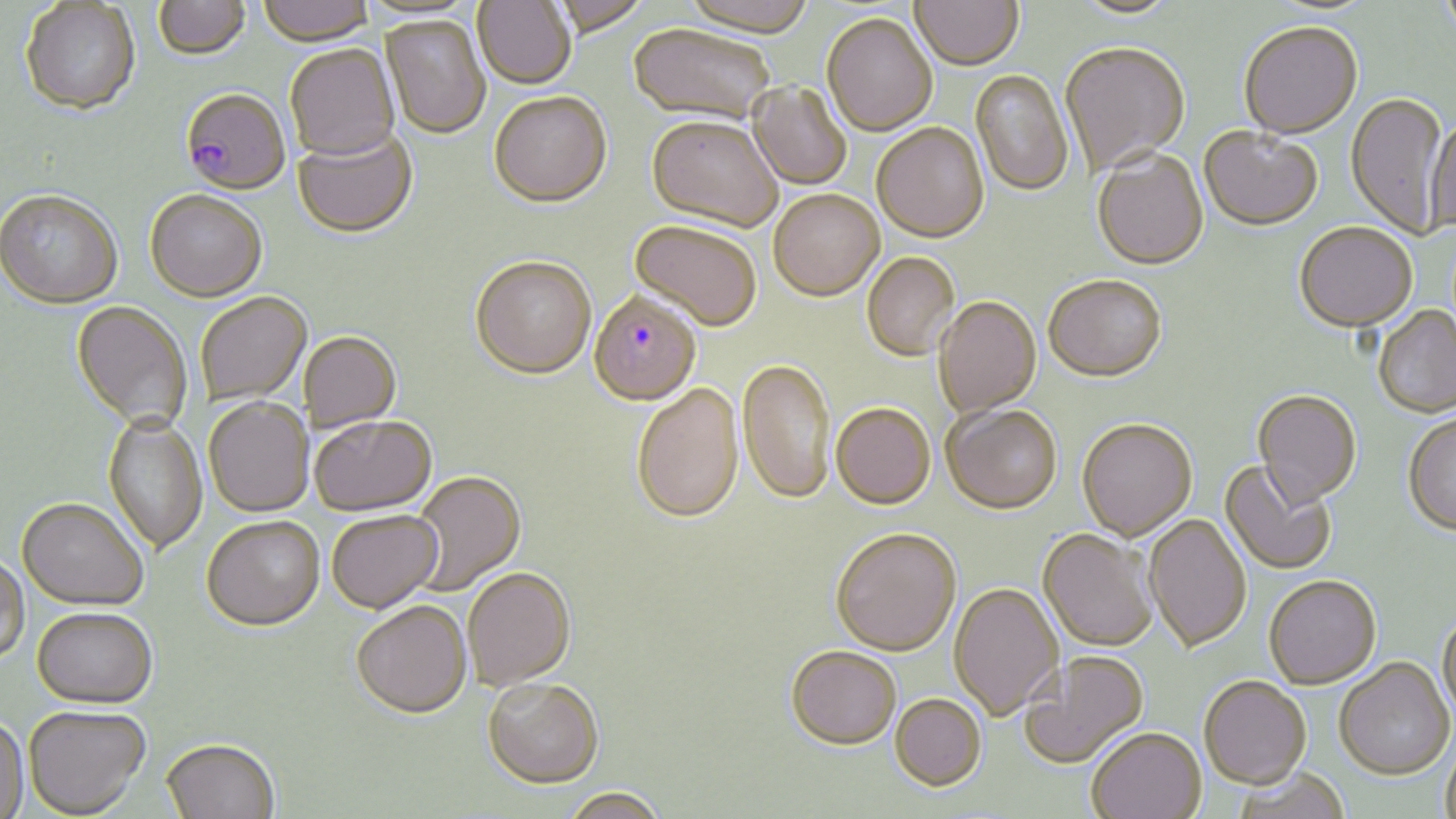
Approximate bounding boxes as [x1, y1, x2, y2] in pixels. Plasmodium falciparum-infected red blood cell locations: [179, 91, 290, 198], [588, 295, 702, 409]. Uninfected red blood cell locations: [256, 0, 376, 48], [472, 0, 576, 91], [680, 0, 819, 40], [910, 0, 1024, 73], [1438, 0, 1456, 44], [153, 1, 251, 62], [1071, 1, 1183, 20], [20, 2, 141, 118], [821, 16, 937, 139], [380, 17, 491, 140], [1239, 24, 1363, 142], [628, 26, 774, 128], [1060, 45, 1190, 178], [285, 47, 401, 164], [970, 70, 1073, 199], [748, 82, 851, 191], [1346, 93, 1449, 240], [490, 95, 612, 211], [1426, 118, 1456, 236], [646, 119, 782, 235], [871, 125, 989, 246], [1199, 129, 1323, 233], [292, 131, 419, 241], [1092, 151, 1209, 272], [0, 193, 123, 312], [145, 193, 267, 305], [769, 193, 884, 304], [628, 222, 761, 335], [1294, 224, 1417, 334], [862, 254, 960, 363], [470, 259, 596, 383], [1043, 278, 1167, 385], [197, 294, 312, 407], [934, 298, 1042, 419], [70, 303, 192, 434], [1374, 306, 1456, 418], [300, 333, 402, 434], [738, 360, 835, 508], [632, 386, 744, 527], [1252, 391, 1362, 510], [203, 400, 314, 519], [831, 406, 935, 512], [942, 407, 1062, 517], [1402, 414, 1456, 537], [102, 415, 208, 557], [311, 418, 438, 520], [1076, 421, 1197, 543], [1220, 459, 1336, 575], [409, 473, 527, 596], [16, 500, 148, 613], [327, 512, 444, 616], [1144, 514, 1251, 654], [202, 519, 326, 635], [1037, 530, 1158, 653], [831, 531, 961, 659], [0, 555, 30, 665], [463, 570, 576, 693], [1264, 575, 1382, 691], [948, 583, 1064, 722], [352, 604, 473, 723], [32, 610, 158, 711], [1437, 610, 1456, 722], [785, 649, 901, 754], [1019, 652, 1150, 770], [1334, 658, 1455, 780], [1199, 677, 1311, 791], [482, 681, 604, 792], [890, 696, 987, 793], [24, 706, 151, 818], [0, 716, 30, 818], [1086, 729, 1207, 819], [1440, 738, 1456, 819], [161, 742, 279, 819], [1232, 770, 1352, 819], [561, 791, 668, 819]. Slide-level diagnosis: Plasmodium falciparum. Thin blood film. One field of a larger specimen. 1000x magnification. May-Grünwald-Giemsa-stained preparation. Image is 1456×819 pixels. Light microscopy.